Give the preparation type.
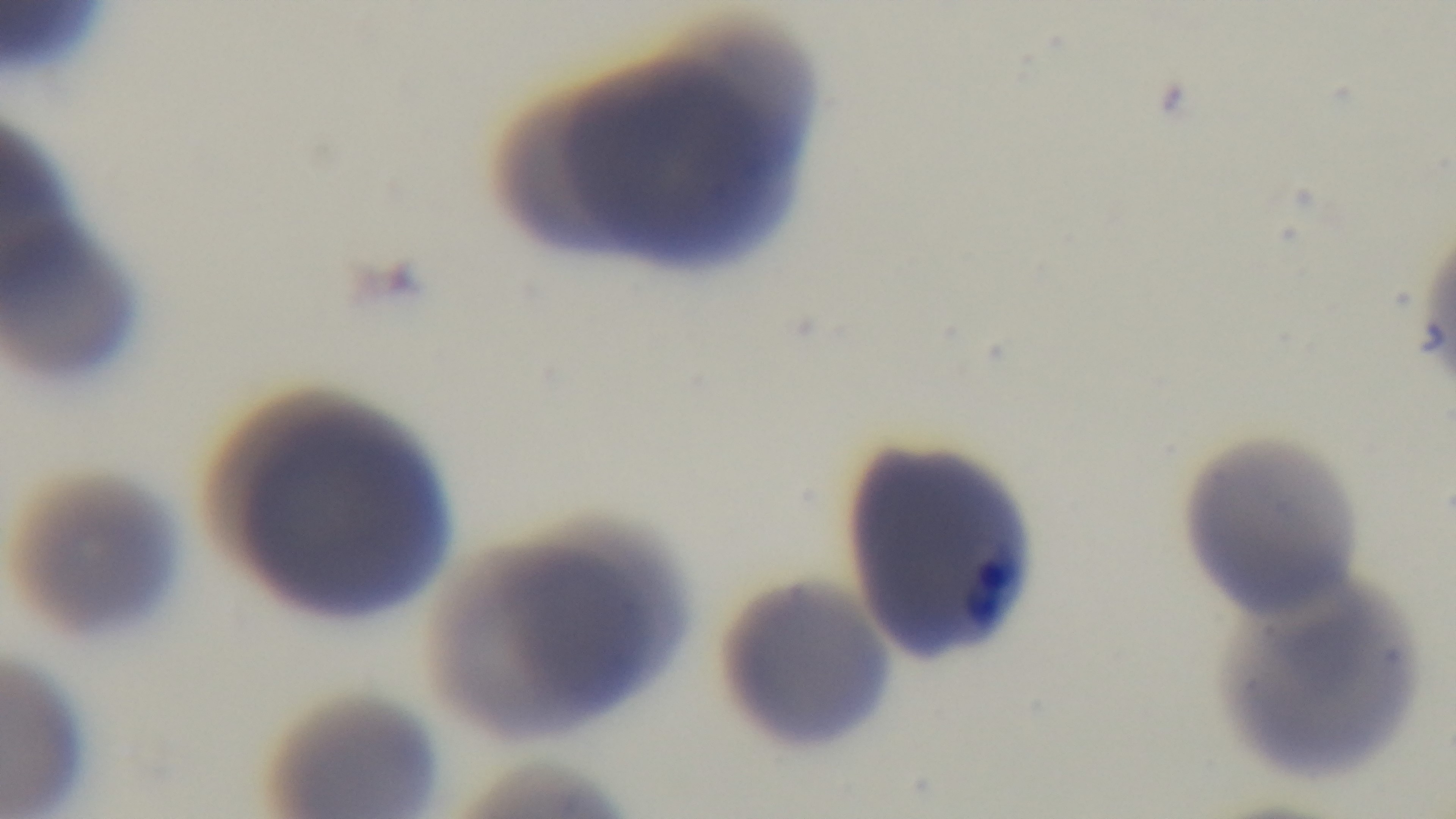
A thin smear.

objective = 100x oil immersion
field of view = one from the slide
malaria status = positive
capture = mounted 4K digital camera
stain = Giemsa
modality = light microscopy